Identify the parasite.
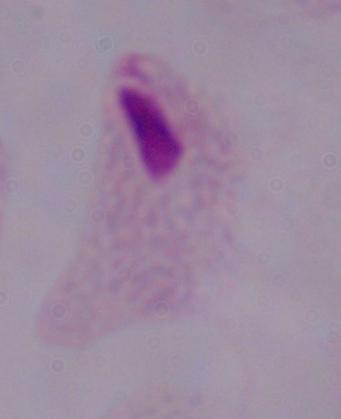
This is a trichomonad.

magnification = 1000x
modality = micrograph